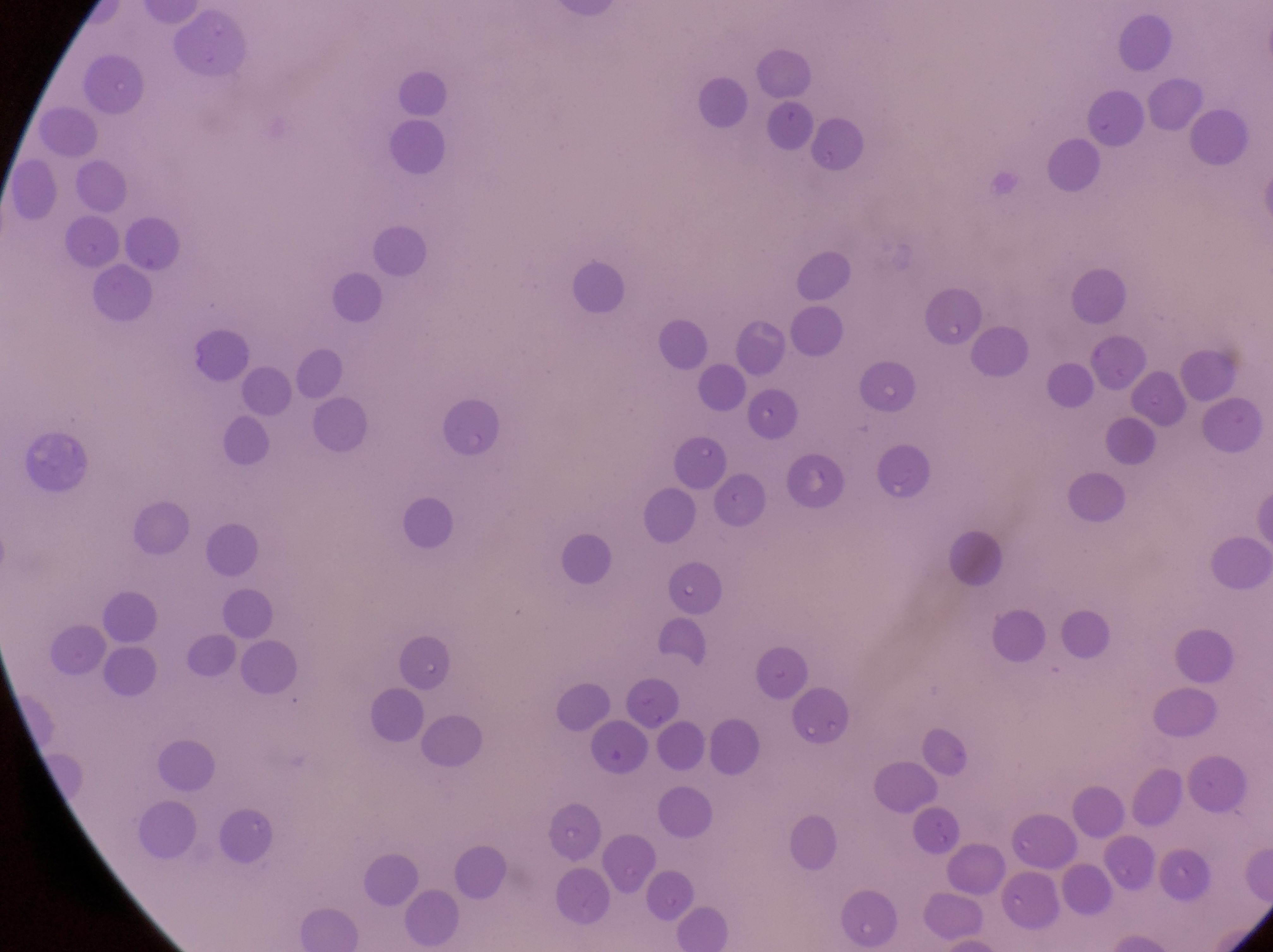
country: Uganda
magnification: 1000x
image_size: 1273×952 pixels
artifact_platelet_like_body_stain_precipitate_or_debris_locations: 'approximate bounding boxes as [left, top, right, bottom] in pixels: [791, 442, 849, 504]'
preparation: thin blood smear
capture: smartphone photograph through the eyepiece of an Olympus CX-23 microscope
field_of_view: single